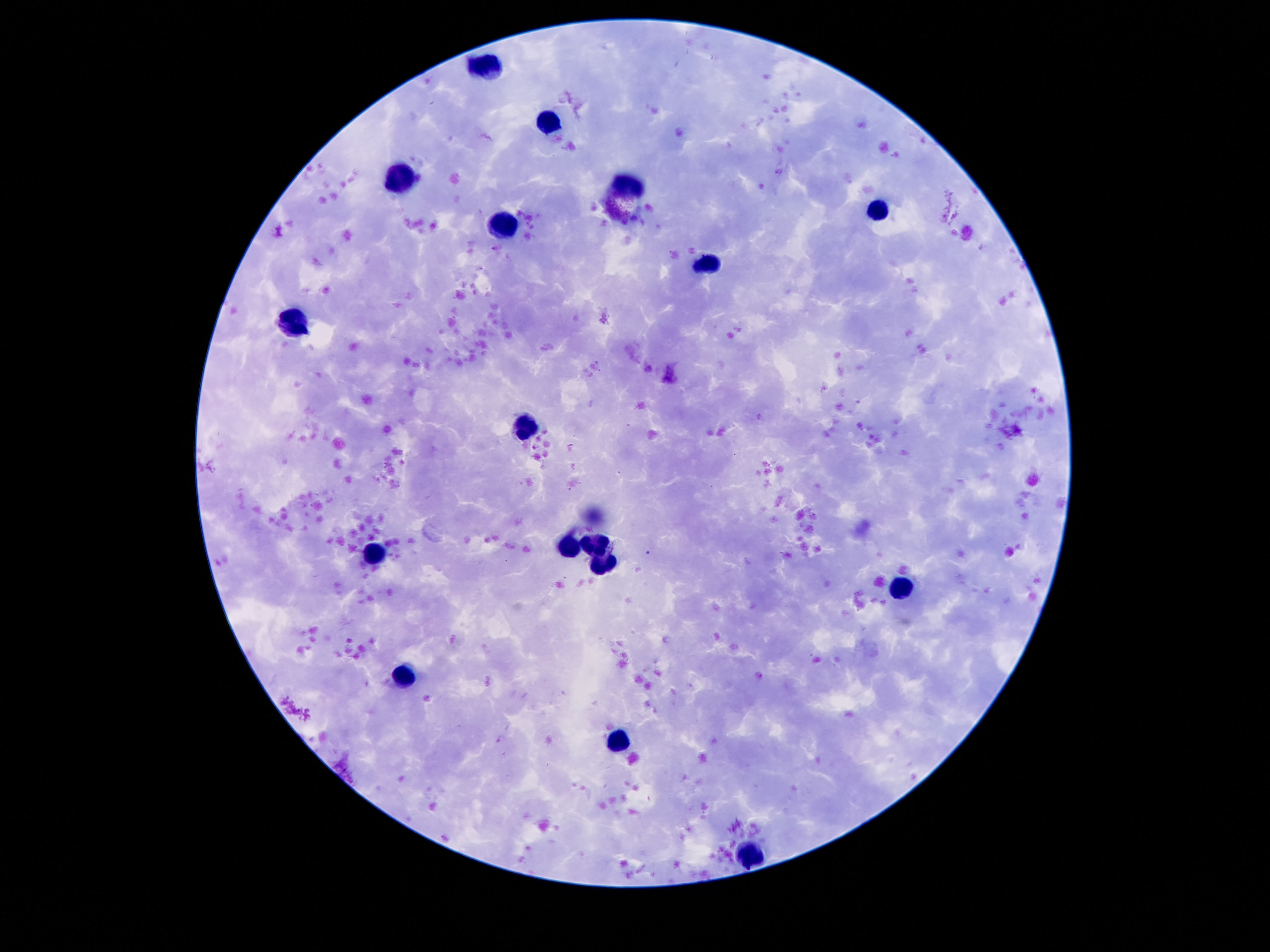
Approximate centers as (x, y) in pixels. Leukocyte locations: (489, 65), (548, 122), (399, 177), (626, 188), (876, 208), (503, 227), (708, 264), (294, 319), (528, 429), (593, 543), (568, 547), (374, 554), (374, 555), (604, 561), (898, 588), (405, 677), (622, 740), (749, 852). Giemsa-stained preparation. 100x magnification. Thick blood film. Photographed through the microscope eyepiece with a smartphone camera. Single field of view. Image is 1270×952 pixels. Patient malaria status: uninfected.